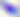
Summary:
  - Identification: Toxoplasma gondii
  - Magnification: 400x
  - Modality: photomicrograph